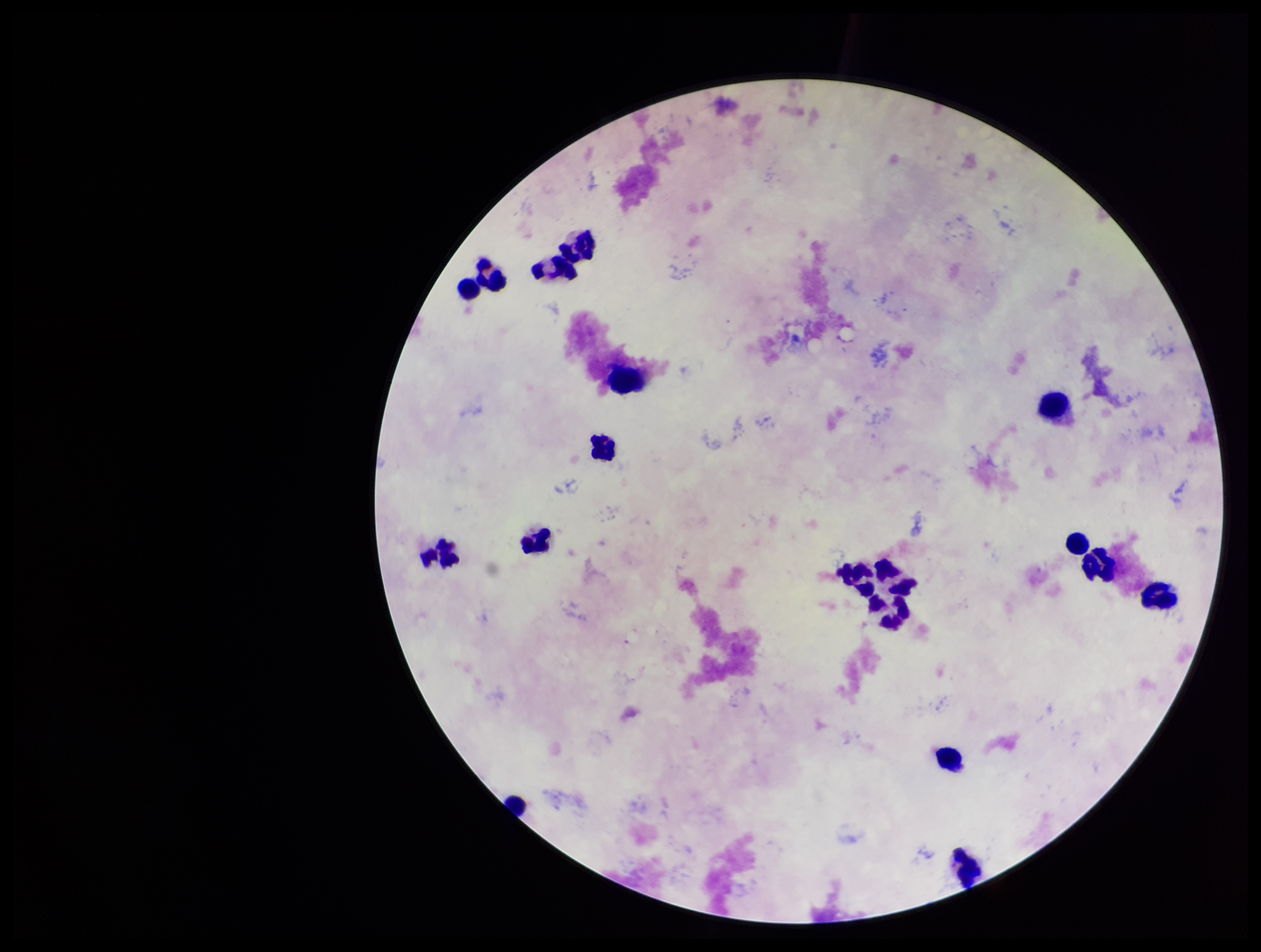

parasite_count: 0
patient_malaria_status: negative
capture: smartphone photograph through the microscope eyepiece
leukocyte_count: 18
plasmodium_parasites: none identified
stain: Giemsa
field_of_view: one from this slide
preparation: thick blood smear
image_size: 1261×952 pixels